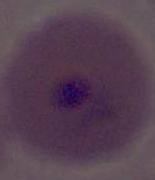

A Plasmodium parasite is shown. Photomicrograph. Captured at either 400x or 1000x magnification.